Classify this cell by malaria status.
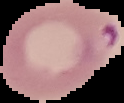
Parasitized.

image type = cell region segmented out of the field of view; surrounding area masked to black
image size = 124×103 pixels
preparation = thin blood film